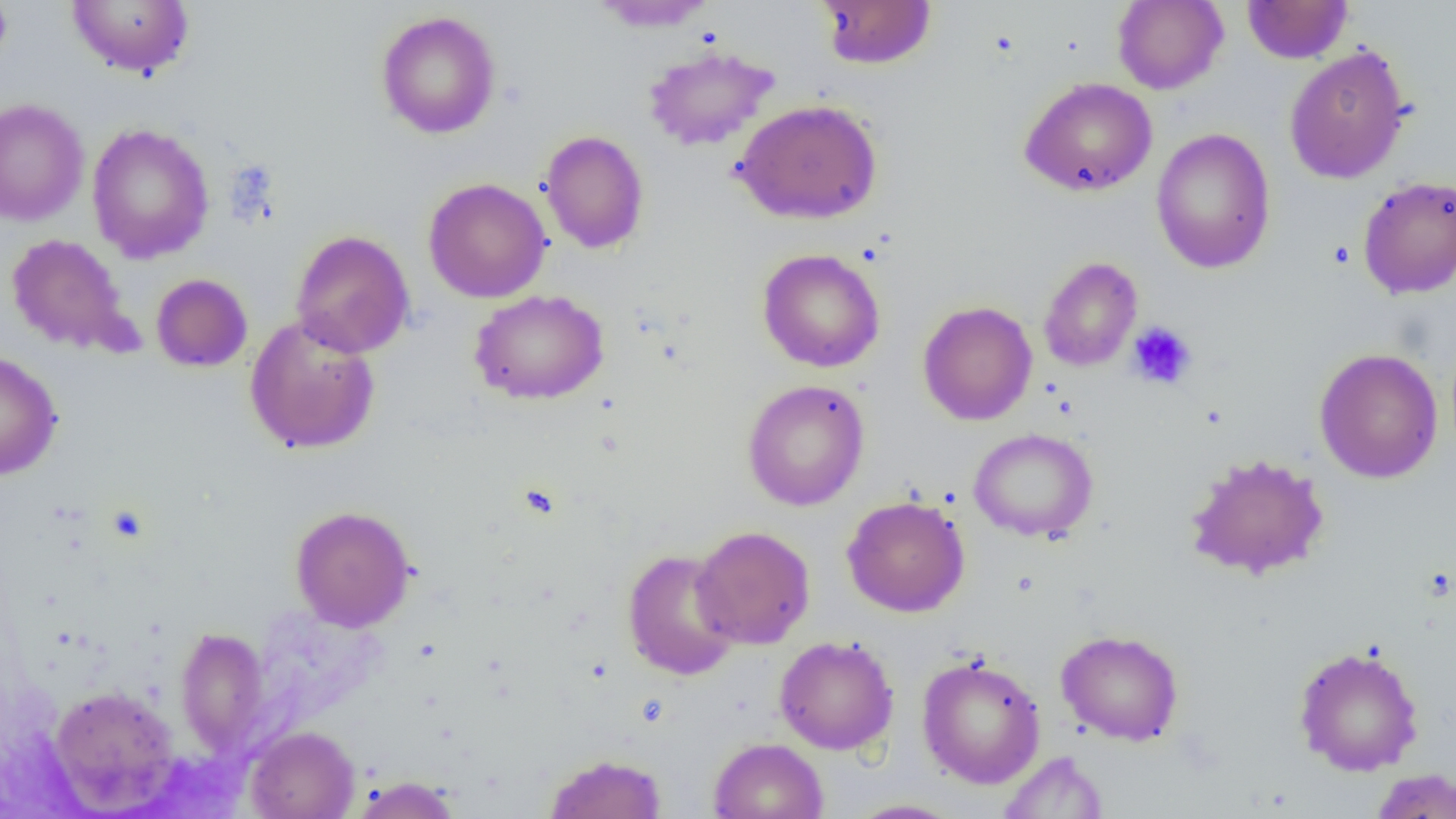

Approximate bounding boxes as named x1/y1/x2/y2 corners in pixels. Uninfected red blood cell locations (subset): (x1=0, y1=0, x2=13, y2=73), (x1=66, y1=0, x2=195, y2=78), (x1=816, y1=0, x2=937, y2=70), (x1=1242, y1=0, x2=1352, y2=64), (x1=590, y1=1, x2=718, y2=32), (x1=1112, y1=1, x2=1228, y2=94), (x1=376, y1=10, x2=501, y2=139), (x1=643, y1=45, x2=779, y2=152), (x1=1284, y1=45, x2=1411, y2=184), (x1=1019, y1=77, x2=1158, y2=198), (x1=0, y1=98, x2=90, y2=227), (x1=731, y1=99, x2=883, y2=225), (x1=86, y1=123, x2=215, y2=264), (x1=1151, y1=128, x2=1276, y2=275), (x1=538, y1=130, x2=650, y2=254), (x1=1358, y1=175, x2=1456, y2=298), (x1=423, y1=178, x2=552, y2=303), (x1=291, y1=229, x2=414, y2=358), (x1=6, y1=234, x2=133, y2=355), (x1=757, y1=248, x2=885, y2=373), (x1=754, y1=250, x2=878, y2=514), (x1=151, y1=273, x2=252, y2=372), (x1=470, y1=289, x2=609, y2=405), (x1=918, y1=300, x2=1037, y2=426), (x1=244, y1=316, x2=381, y2=454), (x1=1314, y1=347, x2=1443, y2=483), (x1=0, y1=350, x2=63, y2=480), (x1=742, y1=379, x2=870, y2=511), (x1=969, y1=428, x2=1098, y2=542), (x1=1185, y1=452, x2=1330, y2=580), (x1=842, y1=496, x2=970, y2=617), (x1=290, y1=505, x2=416, y2=631), (x1=692, y1=525, x2=815, y2=650), (x1=622, y1=549, x2=741, y2=680), (x1=175, y1=626, x2=271, y2=757), (x1=1056, y1=629, x2=1184, y2=746), (x1=774, y1=635, x2=899, y2=755), (x1=1293, y1=644, x2=1425, y2=776), (x1=917, y1=654, x2=1046, y2=789), (x1=49, y1=685, x2=179, y2=812), (x1=246, y1=725, x2=359, y2=819), (x1=709, y1=737, x2=828, y2=819), (x1=998, y1=751, x2=1108, y2=818), (x1=544, y1=753, x2=668, y2=818), (x1=1369, y1=768, x2=1456, y2=818), (x1=351, y1=776, x2=461, y2=818), (x1=845, y1=798, x2=964, y2=818). Platelet locations (subset): (x1=1127, y1=321, x2=1197, y2=390). Slide-level diagnosis: negative for blood parasites. Light microscopy. 1000x magnification. Single field of view. Thin blood film. Image is 1456×819 pixels.